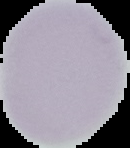
Summary:
  - Result: no malaria parasites seen
  - Image type: cell region segmented out of the field of view; surrounding area masked to black
  - Preparation: thin blood smear
  - Image size: 130×148 pixels